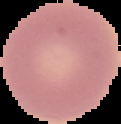

image type = cell region segmented out of the field of view; surrounding area masked to black
malaria status = uninfected
image size = 121×124 pixels
preparation = thin blood film